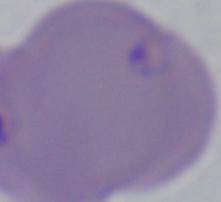
Summary:
  - Modality: photomicrograph
  - Magnification: 1000x
  - Identification: Babesia